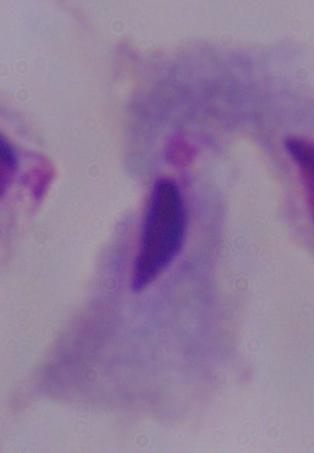

Summary:
  - Magnification: 1000x
  - Identification: trichomonad
  - Modality: micrograph